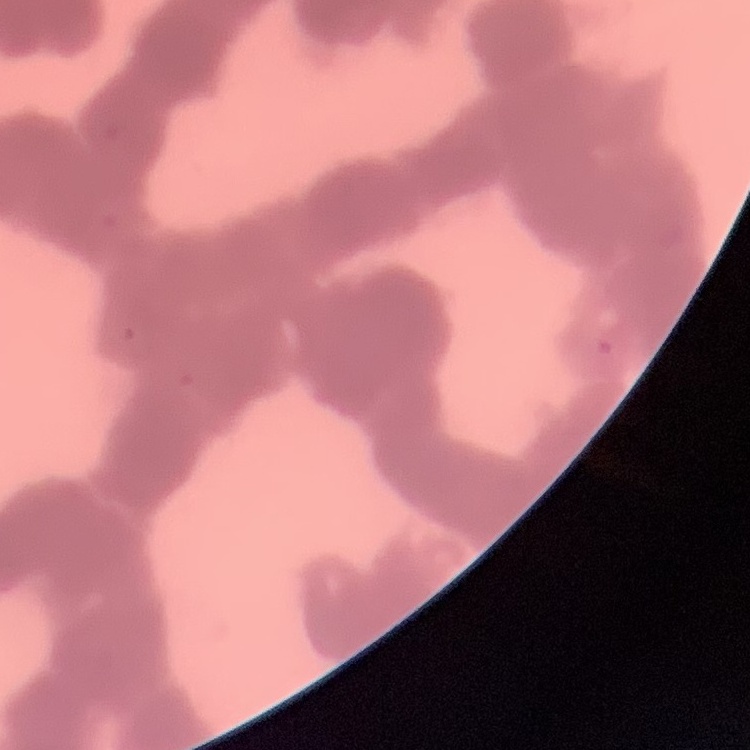
The erythrocytes show rouleaux formation. One tile cut from a larger photomicrograph. Stained with either Field's or Giemsa. Thin blood smear.